Classify this cell by malaria status.
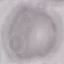
It is uninfected.

image_type: cell patch, automatically extracted from a larger field of view and resized to 64 × 64 pixels
stain: Giemsa
capture: smartphone through the microscope eyepiece
preparation: thin blood smear